Report the malaria status of this cell.
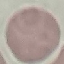
Uninfected.

Photographed with a smartphone camera at the microscope eyepiece. Giemsa-stained preparation. Thin blood smear. Cell patch, automatically extracted from a larger field of view and resized to 64 × 64 pixels.